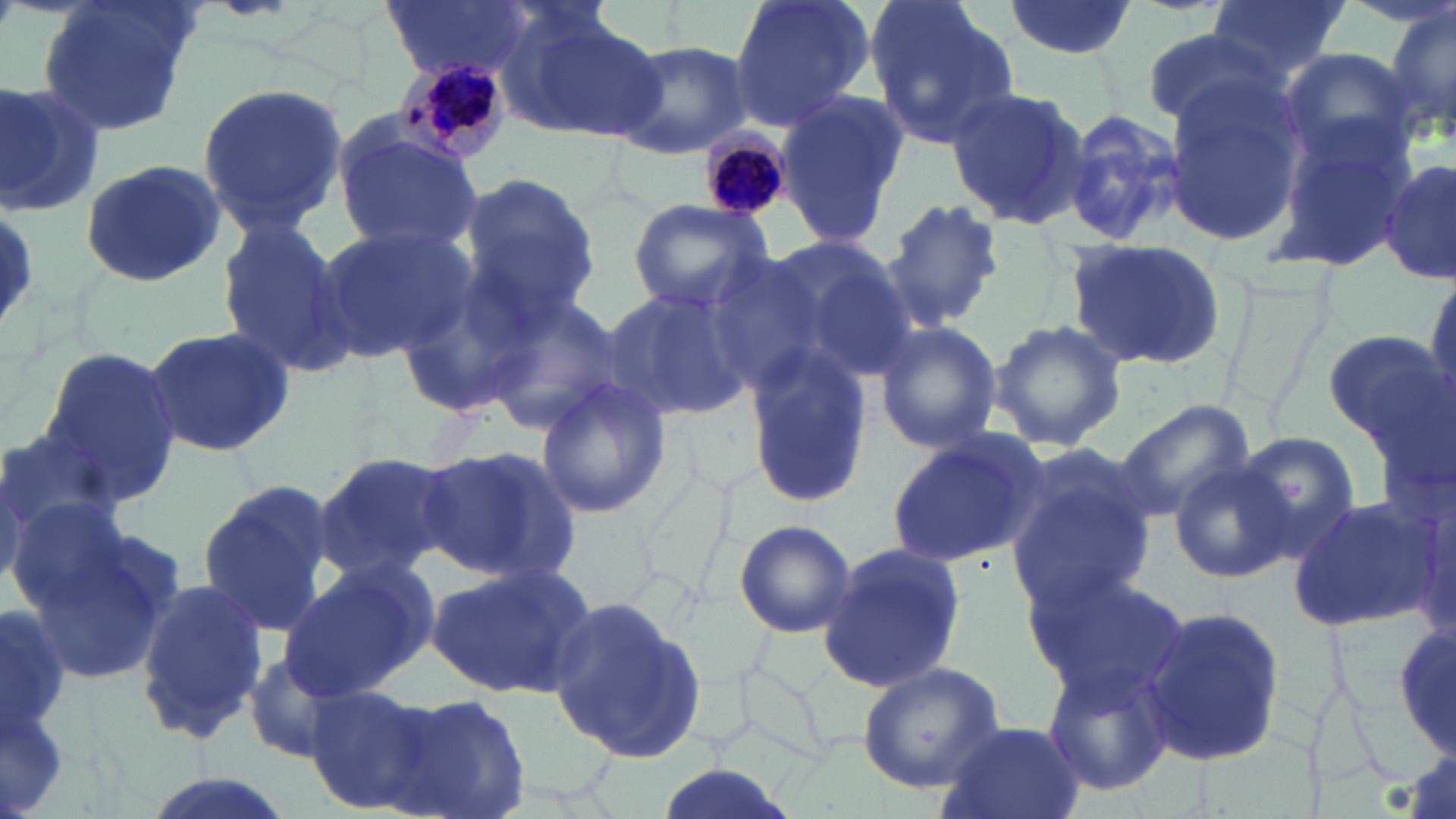

Summary:
  - Coordinate format: approximate bounding boxes as [x1, y1, x2, y2] in pixels
  - Uninfected red blood cell locations: [35, 0, 200, 139], [379, 0, 530, 78], [728, 0, 877, 131], [864, 0, 1017, 144], [1004, 0, 1136, 57], [1204, 0, 1350, 80], [1384, 3, 1455, 143], [495, 7, 659, 143], [1138, 25, 1282, 130], [611, 38, 753, 159], [1277, 46, 1420, 168], [0, 77, 105, 215], [1162, 80, 1310, 251], [195, 81, 348, 233], [943, 84, 1090, 228], [772, 91, 908, 249], [1053, 106, 1188, 249], [333, 119, 483, 255], [1266, 127, 1416, 277], [1380, 157, 1455, 283], [79, 159, 232, 286], [457, 171, 600, 318], [881, 196, 1005, 328], [625, 198, 772, 313], [216, 219, 358, 380], [313, 224, 471, 363], [749, 236, 920, 388], [1063, 237, 1228, 373], [694, 252, 826, 392], [1424, 269, 1456, 406], [600, 289, 753, 424], [481, 291, 630, 434], [987, 318, 1127, 450], [873, 320, 1003, 455], [143, 325, 296, 460], [1321, 330, 1449, 446], [37, 344, 183, 506], [746, 347, 875, 509], [535, 377, 671, 520], [1118, 400, 1256, 518], [1, 429, 126, 554], [884, 433, 1043, 570], [1233, 433, 1358, 560], [418, 443, 583, 588], [1004, 444, 1162, 608], [313, 450, 458, 580], [1170, 460, 1293, 584], [196, 479, 337, 637], [1286, 491, 1440, 635], [17, 504, 179, 686], [733, 519, 857, 638], [742, 524, 940, 664], [819, 540, 970, 693], [424, 563, 594, 700], [274, 565, 428, 704], [1022, 565, 1187, 700], [133, 578, 266, 742], [545, 593, 706, 764], [1138, 605, 1287, 770], [1394, 624, 1455, 761], [239, 651, 356, 764], [1040, 660, 1177, 798], [856, 662, 1010, 794], [303, 684, 438, 813], [394, 694, 532, 818], [935, 720, 1085, 819], [648, 763, 804, 819], [136, 773, 297, 819]
  - Plasmodium malariae-infected red blood cell locations: [392, 50, 517, 164], [701, 123, 794, 224]
  - Slide-level diagnosis: Plasmodium malariae
  - Field of view: one of a larger specimen
  - Modality: optical microscopy
  - Stain: May-Grünwald-Giemsa
  - Image size: 1456×819 pixels
  - Preparation: thin blood film
  - Magnification: 1000x